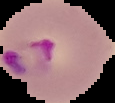
From a thin blood film. Segmented cell region on a black background. Result: Plasmodium parasites identified. Image is 115×103 pixels.